Assess this cell for malaria.
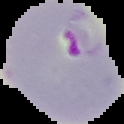
Parasitized.

image type = segmented cell region on a black background
image size = 124×124 pixels
preparation = thin blood film